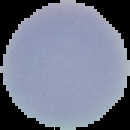
Malaria status: uninfected. From a thin blood film. Image is 130×130 pixels. The area outside the segmented cell region is set to black.